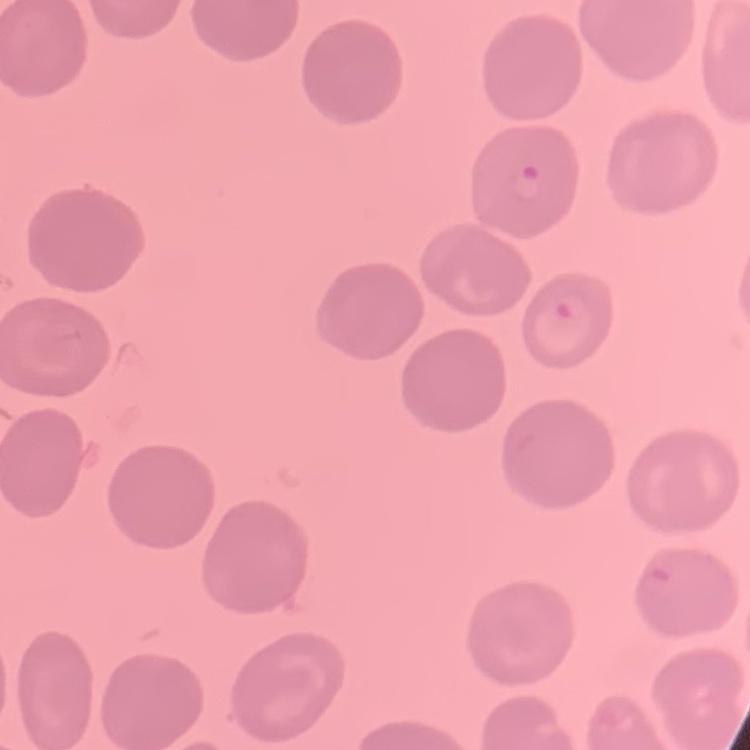

erythrocyte morphology = no rouleaux formation
preparation = thin blood smear
image type = square crop of a larger photomicrograph
stain = Field's or Giemsa